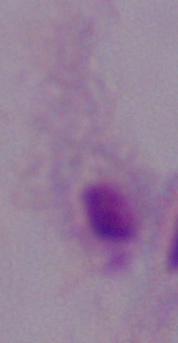

magnification = 1000x
modality = photomicrograph
identification = trichomonad